Report the malaria status of this cell.
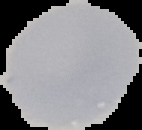

Uninfected.

Summary:
  - Preparation: thin blood film
  - Image type: segmented cell region with the area outside set to black
  - Image size: 142×130 pixels